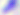
magnification = 400x
identification = Toxoplasma gondii
modality = micrograph